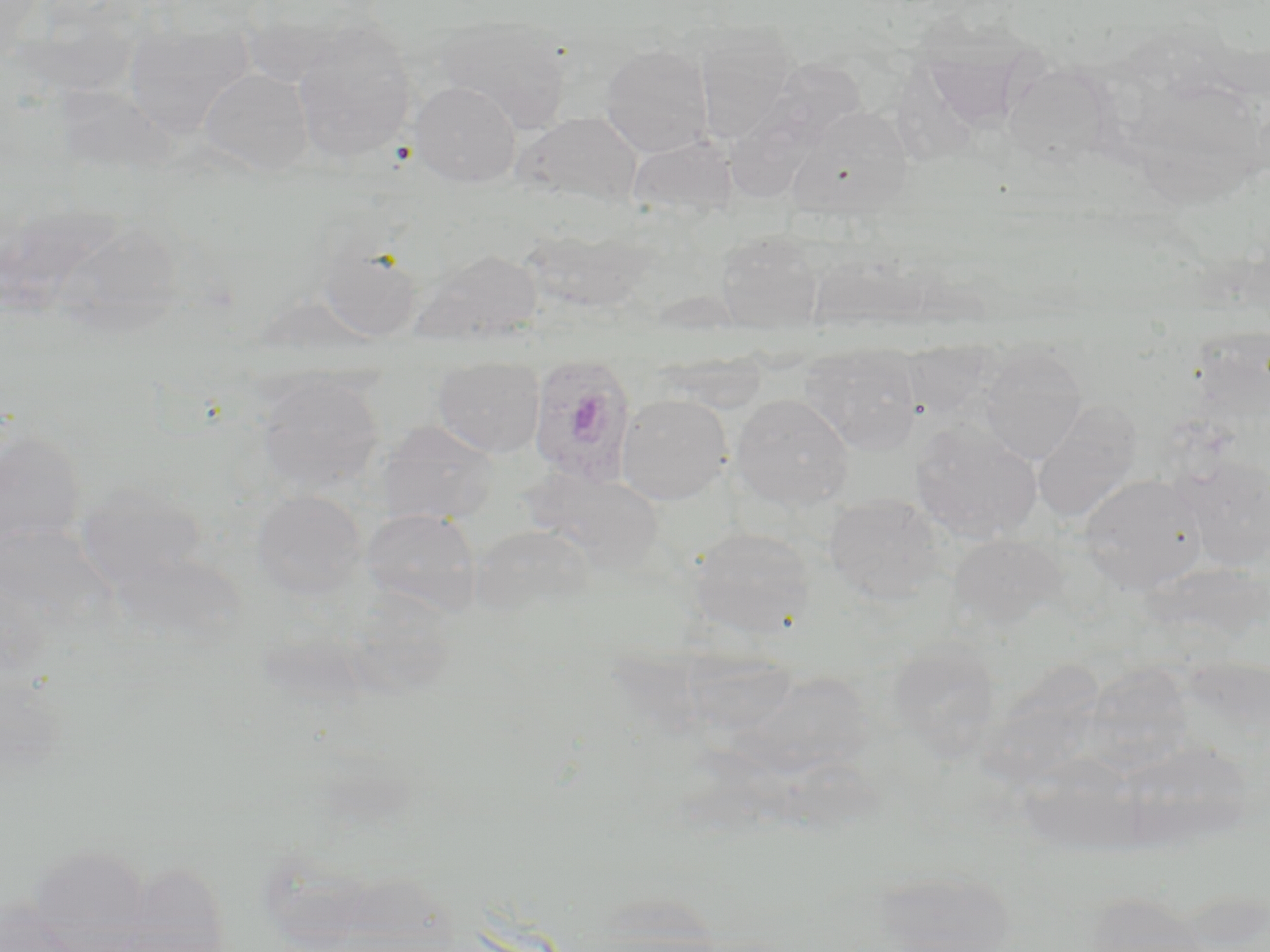

slide_level_diagnosis: Plasmodium ovale
uninfected_red_blood_cell_locations: 'approximate bounding boxes as named x1/y1/x2/y2 corners in pixels: (x1=435, y1=14, x2=572, y2=131), (x1=124, y1=19, x2=253, y2=140), (x1=292, y1=23, x2=417, y2=164), (x1=692, y1=25, x2=801, y2=144), (x1=600, y1=43, x2=714, y2=157), (x1=753, y1=57, x2=867, y2=157), (x1=1003, y1=62, x2=1111, y2=171), (x1=198, y1=68, x2=314, y2=176), (x1=410, y1=81, x2=521, y2=187), (x1=1151, y1=83, x2=1256, y2=213), (x1=787, y1=106, x2=913, y2=220), (x1=516, y1=112, x2=644, y2=208), (x1=627, y1=134, x2=738, y2=221), (x1=60, y1=220, x2=191, y2=347), (x1=715, y1=231, x2=824, y2=333), (x1=318, y1=240, x2=423, y2=342), (x1=414, y1=248, x2=542, y2=345), (x1=903, y1=340, x2=993, y2=417), (x1=801, y1=344, x2=922, y2=455), (x1=978, y1=346, x2=1088, y2=465), (x1=433, y1=357, x2=544, y2=458), (x1=256, y1=373, x2=385, y2=495), (x1=616, y1=393, x2=733, y2=504), (x1=730, y1=393, x2=855, y2=510), (x1=1031, y1=400, x2=1141, y2=525), (x1=377, y1=421, x2=500, y2=526), (x1=910, y1=422, x2=1042, y2=542), (x1=0, y1=424, x2=87, y2=552), (x1=1176, y1=455, x2=1270, y2=570), (x1=522, y1=467, x2=665, y2=574), (x1=1079, y1=473, x2=1207, y2=593), (x1=76, y1=481, x2=210, y2=591), (x1=251, y1=489, x2=367, y2=601), (x1=824, y1=493, x2=945, y2=605), (x1=361, y1=507, x2=482, y2=618), (x1=471, y1=524, x2=595, y2=618), (x1=688, y1=527, x2=816, y2=638), (x1=948, y1=533, x2=1068, y2=634), (x1=886, y1=638, x2=1002, y2=761), (x1=993, y1=654, x2=1108, y2=777), (x1=1090, y1=657, x2=1202, y2=780), (x1=721, y1=669, x2=881, y2=786), (x1=1110, y1=738, x2=1254, y2=854), (x1=1018, y1=752, x2=1145, y2=858), (x1=27, y1=845, x2=152, y2=948), (x1=870, y1=868, x2=1020, y2=952), (x1=1083, y1=893, x2=1215, y2=952), (x1=0, y1=901, x2=86, y2=952)'
modality: optical microscopy
preparation: thin blood smear
magnification: 1000x
image_size: 1270×952 pixels
field_of_view: one of a larger specimen
stain: May-Grünwald-Giemsa
plasmodium_ovale_infected_red_blood_cell_locations: 'approximate bounding boxes as named x1/y1/x2/y2 corners in pixels: (x1=528, y1=355, x2=637, y2=490)'